Classify this cell by malaria status.
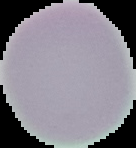
Uninfected.

Summary:
  - Image size: 136×148 pixels
  - Preparation: thin blood smear
  - Image type: cell region segmented out of the field of view; surrounding area masked to black